Outline each Plasmodium malariae-infected red blood cell.
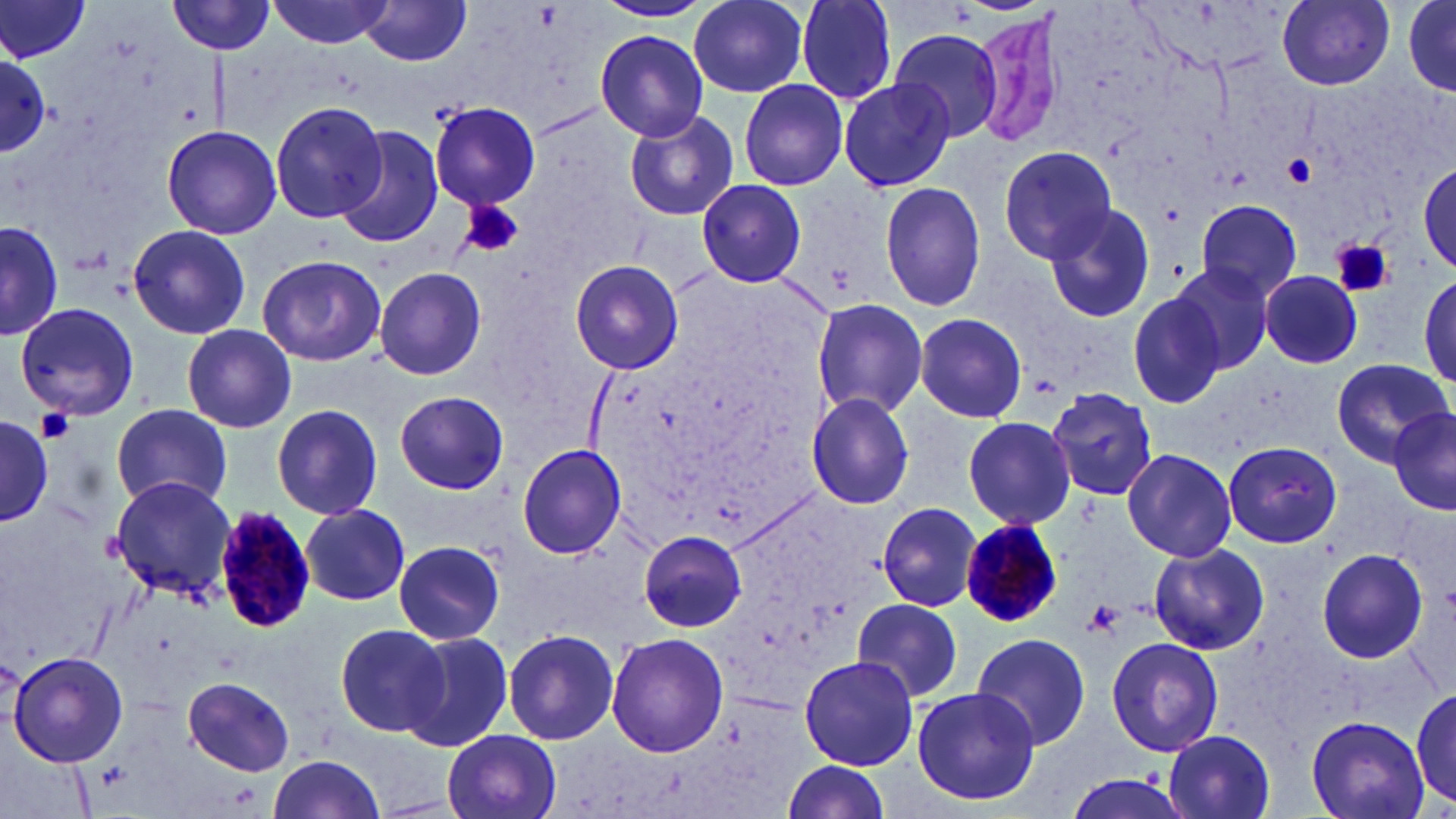
Approximate bounding boxes as [x1, y1, x2, y2] in pixels.
Plasmodium malariae-infected red blood cells: [211, 504, 321, 636], [956, 514, 1061, 629].

Platelet locations: [1281, 151, 1318, 187], [460, 202, 525, 258], [1333, 239, 1393, 298], [37, 408, 75, 442], [1087, 599, 1123, 634]. Uninfected red blood cell locations: [267, 0, 399, 48], [795, 0, 898, 104], [1278, 0, 1395, 90], [0, 1, 91, 61], [167, 1, 279, 56], [363, 1, 470, 67], [587, 1, 716, 24], [689, 1, 809, 97], [1402, 1, 1455, 97], [1401, 3, 1456, 93], [968, 12, 1074, 149], [595, 29, 710, 141], [888, 29, 1004, 144], [0, 52, 50, 153], [838, 78, 955, 192], [737, 79, 848, 191], [430, 100, 540, 210], [268, 101, 388, 223], [624, 110, 738, 221], [162, 125, 282, 240], [334, 127, 444, 248], [997, 145, 1119, 264], [1418, 160, 1456, 273], [697, 179, 807, 288], [879, 181, 987, 313], [1195, 198, 1304, 301], [1041, 202, 1157, 325], [1186, 206, 1322, 370], [1, 219, 61, 342], [126, 224, 252, 340], [256, 254, 387, 367], [568, 259, 685, 375], [1170, 261, 1276, 373], [375, 267, 486, 381], [1261, 270, 1365, 368], [1417, 274, 1455, 396], [1127, 291, 1227, 408], [811, 297, 928, 419], [15, 301, 142, 421], [914, 313, 1027, 422], [182, 324, 297, 433], [1331, 357, 1450, 464], [1047, 384, 1160, 500], [1048, 386, 1157, 499], [394, 391, 509, 494], [807, 392, 915, 511], [112, 404, 233, 512], [272, 404, 383, 520], [1387, 405, 1456, 516], [0, 414, 51, 525], [962, 415, 1077, 529], [1224, 440, 1342, 547], [516, 443, 627, 559], [1121, 448, 1237, 562], [109, 475, 236, 600], [877, 502, 982, 611], [301, 505, 409, 605], [639, 530, 746, 634], [393, 540, 505, 645], [1147, 543, 1269, 656], [1316, 548, 1430, 664], [853, 597, 963, 704], [334, 623, 448, 739], [399, 629, 513, 752], [503, 629, 620, 745], [605, 632, 729, 757], [971, 632, 1091, 752], [1105, 635, 1225, 756], [7, 649, 129, 767], [799, 655, 918, 770], [182, 676, 295, 775], [1413, 685, 1454, 812], [912, 689, 1039, 807], [1306, 714, 1430, 819], [443, 730, 562, 819], [1162, 730, 1277, 819], [266, 754, 387, 819], [781, 757, 891, 819], [1062, 770, 1194, 819]. Slide-level diagnosis: Plasmodium malariae. Captured at 1000x magnification. Image is 1456×819 pixels. Optical microscopy. One field of a larger specimen. Thin blood film. May-Grünwald-Giemsa stain.